Classify the preparation.
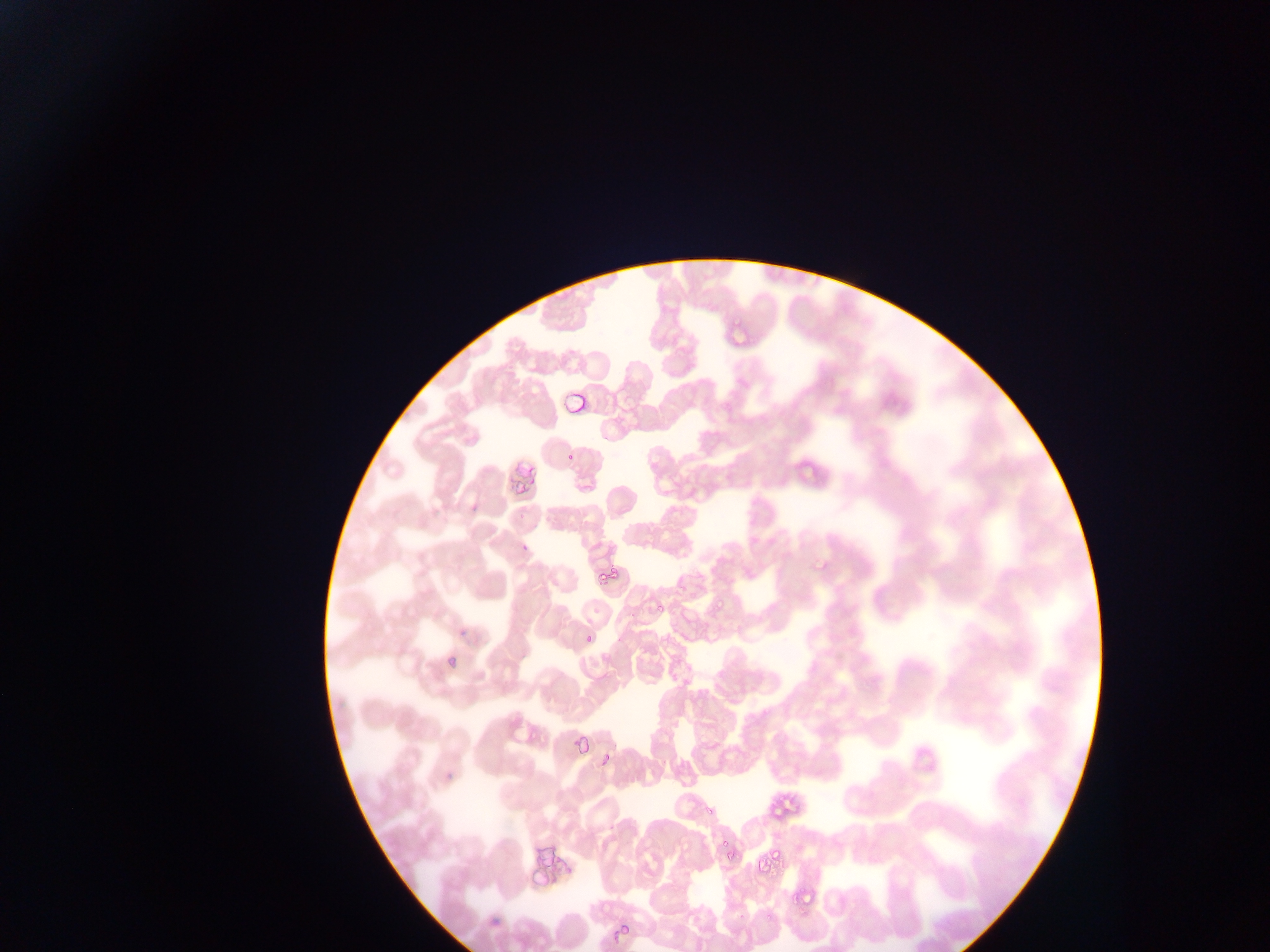
This is a thin smear.

Approximate bounding boxes as left top right bottom in pixels.
Summary:
  - Malaria parasite locations: 731 317 747 327; 558 389 587 420; 565 450 576 465; 813 558 830 575; 613 567 625 585; 594 569 608 586; 652 598 668 614; 711 598 729 613; 455 620 471 639; 581 636 593 645; 573 722 594 750; 599 749 616 766; 699 805 714 817; 716 832 736 849; 723 846 742 863; 769 849 789 863; 801 893 813 910; 788 897 797 909; 764 914 773 924; 618 919 632 937
  - Field of view: single
  - Capture: mobile-phone photograph through a microscope
  - Country: Ghana
  - Image size: 1270×952 pixels